State which cell type is depicted.
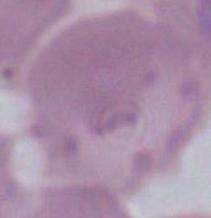
This is an erythrocyte.

{
  "modality": "photomicrograph",
  "magnification": "1000x"
}